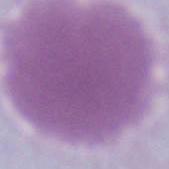 A red blood cell is seen. Micrograph. 1000x magnification.